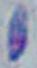

Summary:
  - Identification: Toxoplasma gondii
  - Magnification: 1000x
  - Modality: micrograph